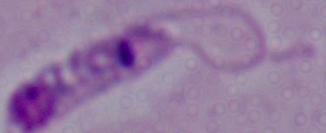

A Leishmania parasite is seen. Photomicrograph. Captured at 1000x magnification.